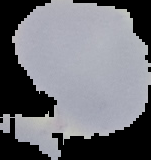

Summary:
  - Preparation: thin blood film
  - Result: negative for malaria parasites
  - Image size: 151×160 pixels
  - Image type: segmented cell region on a black background